State the blood parasite species.
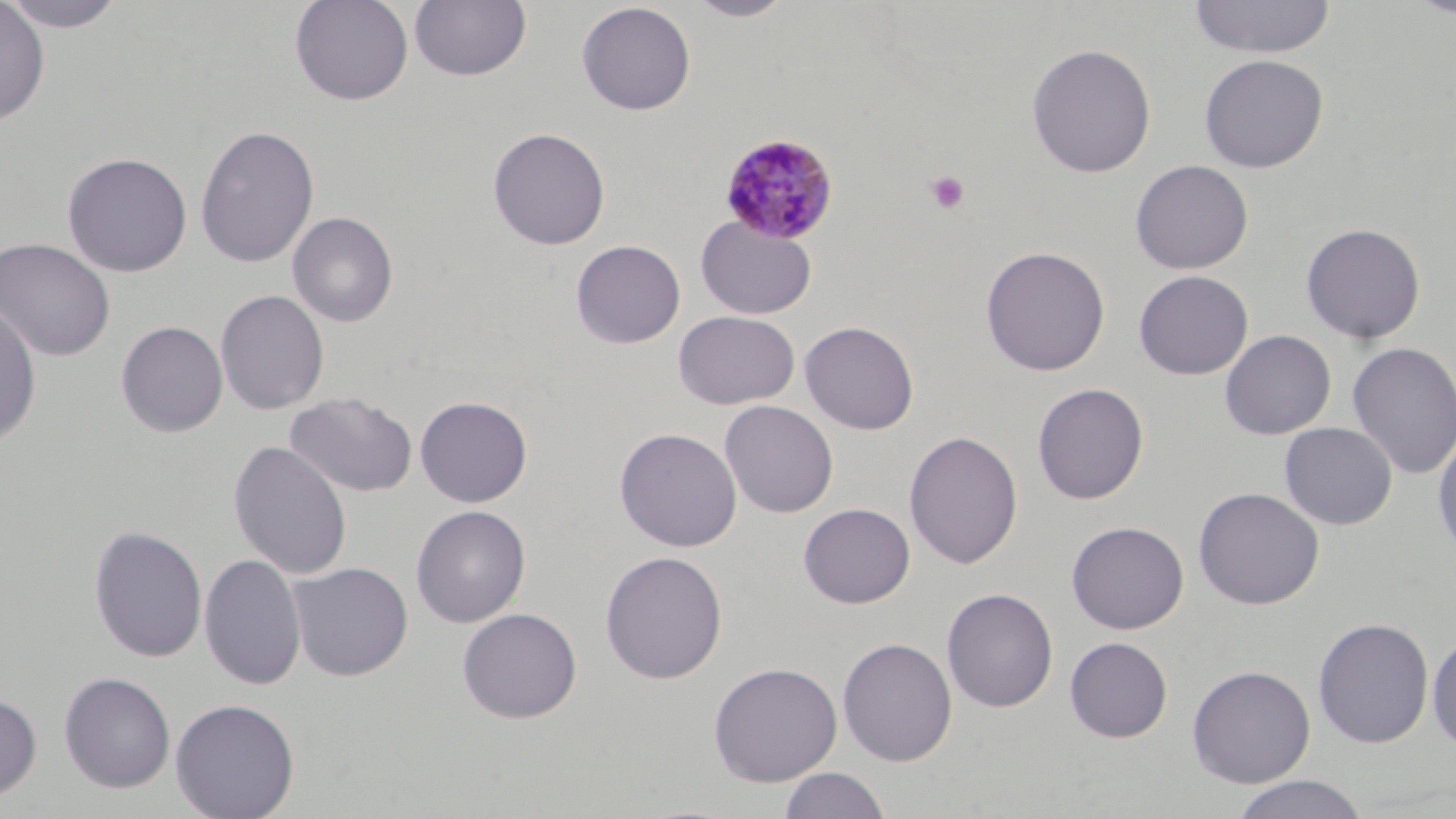
Plasmodium malariae.

field_of_view: one of a larger specimen
platelet_locations: 'approximate bounding boxes as named x1/y1/x2/y2 corners in pixels: (x1=925, y1=171, x2=970, y2=215)'
stain: May-Grünwald-Giemsa
modality: light microscopy
plasmodium_malariae_infected_red_blood_cell_locations: 'approximate bounding boxes as named x1/y1/x2/y2 corners in pixels: (x1=718, y1=132, x2=840, y2=244)'
image_size: 1456×819 pixels
magnification: 1000x
uninfected_red_blood_cell_locations: 'approximate bounding boxes as named x1/y1/x2/y2 corners in pixels: (x1=2, y1=0, x2=131, y2=32), (x1=290, y1=0, x2=414, y2=106), (x1=409, y1=0, x2=531, y2=82), (x1=685, y1=0, x2=796, y2=21), (x1=1188, y1=0, x2=1337, y2=59), (x1=1407, y1=0, x2=1456, y2=19), (x1=0, y1=1, x2=50, y2=126), (x1=576, y1=2, x2=696, y2=115), (x1=1026, y1=43, x2=1157, y2=178), (x1=1199, y1=54, x2=1329, y2=173), (x1=195, y1=124, x2=320, y2=268), (x1=487, y1=127, x2=611, y2=250), (x1=61, y1=151, x2=193, y2=277), (x1=1130, y1=159, x2=1253, y2=273), (x1=288, y1=211, x2=398, y2=327), (x1=696, y1=216, x2=817, y2=319), (x1=1300, y1=222, x2=1426, y2=344), (x1=0, y1=237, x2=116, y2=362), (x1=570, y1=239, x2=686, y2=348), (x1=980, y1=245, x2=1110, y2=376), (x1=1134, y1=270, x2=1253, y2=380), (x1=214, y1=289, x2=329, y2=415), (x1=0, y1=301, x2=41, y2=447), (x1=673, y1=310, x2=800, y2=409), (x1=116, y1=320, x2=228, y2=437), (x1=799, y1=320, x2=920, y2=435), (x1=1220, y1=330, x2=1336, y2=439), (x1=1347, y1=341, x2=1456, y2=480), (x1=1032, y1=382, x2=1149, y2=504), (x1=285, y1=392, x2=418, y2=497), (x1=415, y1=395, x2=533, y2=507), (x1=720, y1=400, x2=838, y2=518), (x1=1279, y1=422, x2=1397, y2=529), (x1=614, y1=427, x2=742, y2=552), (x1=1432, y1=429, x2=1456, y2=561), (x1=904, y1=430, x2=1023, y2=570), (x1=229, y1=441, x2=352, y2=579), (x1=1192, y1=487, x2=1325, y2=610), (x1=798, y1=503, x2=916, y2=608), (x1=410, y1=504, x2=531, y2=627), (x1=1066, y1=521, x2=1189, y2=634), (x1=89, y1=525, x2=208, y2=663), (x1=600, y1=550, x2=728, y2=684), (x1=200, y1=554, x2=306, y2=690), (x1=289, y1=562, x2=413, y2=681), (x1=942, y1=587, x2=1058, y2=712), (x1=457, y1=607, x2=582, y2=724), (x1=1313, y1=617, x2=1434, y2=748), (x1=1427, y1=630, x2=1456, y2=753), (x1=1064, y1=636, x2=1173, y2=742), (x1=837, y1=637, x2=958, y2=766), (x1=708, y1=661, x2=843, y2=786), (x1=1186, y1=665, x2=1316, y2=787), (x1=58, y1=671, x2=176, y2=793), (x1=0, y1=691, x2=42, y2=802), (x1=169, y1=697, x2=300, y2=819), (x1=778, y1=767, x2=892, y2=819), (x1=1230, y1=774, x2=1370, y2=819)'
preparation: thin blood film